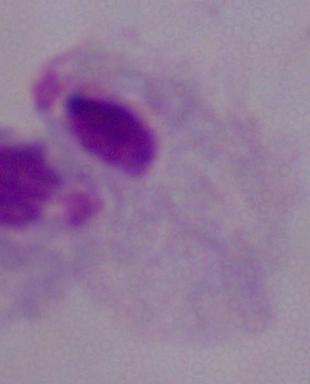
modality = photomicrograph
identification = trichomonad
magnification = 1000x